Outline each blood parasite and name the species.
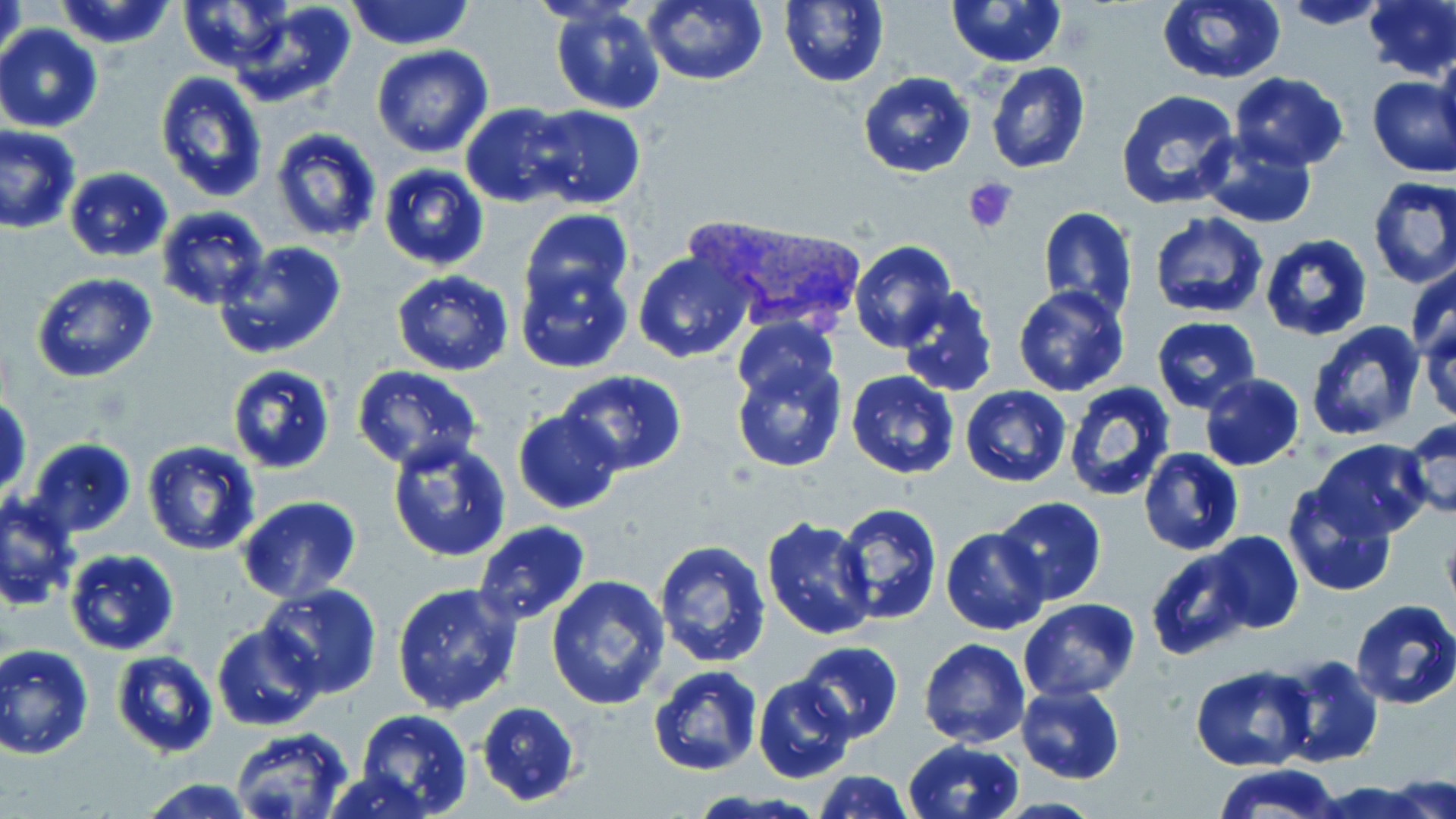
Approximate bounding boxes as (x1, y1, x2, y2) in pixels.
Plasmodium vivax-infected red blood cells: (685, 214, 861, 340).
No Plasmodium falciparum, Plasmodium ovale, Plasmodium malariae, Babesia divergens, or Trypanosoma brucei observed.

Summary:
  - Uninfected red blood cell locations: (52, 0, 180, 51), (177, 0, 296, 71), (228, 0, 356, 108), (345, 0, 475, 50), (642, 0, 768, 86), (778, 0, 889, 87), (946, 0, 1070, 68), (1278, 0, 1394, 30), (1155, 1, 1287, 85), (1363, 1, 1456, 80), (1, 2, 28, 72), (548, 3, 665, 115), (0, 25, 103, 132), (1435, 44, 1456, 161), (371, 45, 494, 158), (984, 61, 1091, 174), (857, 71, 977, 179), (154, 72, 268, 203), (1230, 72, 1349, 168), (1365, 76, 1455, 179), (1114, 89, 1241, 213), (460, 103, 582, 207), (528, 106, 645, 209), (0, 125, 82, 234), (270, 127, 383, 243), (1195, 131, 1319, 227), (376, 164, 490, 271), (63, 167, 173, 261), (1367, 176, 1456, 290), (155, 205, 270, 310), (1038, 206, 1138, 320), (519, 209, 634, 312), (1149, 213, 1270, 320), (1259, 233, 1373, 342), (213, 241, 347, 361), (850, 241, 955, 352), (633, 249, 757, 364), (515, 258, 634, 373), (1407, 262, 1456, 362), (391, 270, 514, 377), (32, 272, 158, 384), (896, 284, 999, 397), (1012, 285, 1131, 397), (1419, 315, 1456, 426), (1152, 316, 1259, 412), (733, 318, 839, 406), (1302, 320, 1428, 441), (730, 355, 848, 474), (225, 363, 336, 475), (353, 366, 482, 474), (556, 370, 688, 476), (845, 370, 960, 479), (1199, 374, 1304, 470), (1063, 380, 1177, 502), (959, 385, 1070, 488), (1, 397, 30, 502), (513, 411, 621, 514), (1401, 417, 1456, 522), (25, 438, 138, 537), (386, 438, 512, 562), (1309, 438, 1432, 541), (142, 439, 262, 556), (1138, 447, 1245, 558), (1282, 487, 1395, 597), (1, 493, 81, 610), (236, 495, 362, 604), (991, 496, 1107, 605), (833, 503, 941, 624), (760, 518, 878, 641), (473, 521, 590, 625), (942, 527, 1050, 635), (1202, 531, 1302, 634), (653, 538, 774, 669), (1146, 546, 1252, 660), (65, 549, 178, 655), (546, 575, 670, 710), (391, 582, 523, 714), (257, 584, 383, 697), (1019, 598, 1139, 701), (1350, 598, 1456, 708), (213, 622, 323, 731), (919, 638, 1030, 749), (793, 641, 903, 744), (1, 643, 94, 758), (112, 650, 218, 757), (1273, 654, 1384, 768), (1190, 664, 1314, 771), (646, 665, 762, 776), (753, 675, 857, 785), (1015, 683, 1127, 783), (476, 701, 581, 805), (354, 709, 472, 819), (230, 729, 356, 816), (904, 739, 1024, 819), (1212, 765, 1346, 819), (323, 770, 439, 818), (811, 771, 914, 818), (1386, 774, 1454, 819), (138, 777, 257, 818), (1317, 780, 1433, 819)
  - Platelet locations: (964, 176, 1021, 232)
  - Slide-level diagnosis: Plasmodium vivax
  - Magnification: 1000x
  - Modality: light microscopy
  - Preparation: thin blood smear
  - Field of view: one of a larger specimen
  - Image size: 1456×819 pixels
  - Stain: May-Grünwald-Giemsa